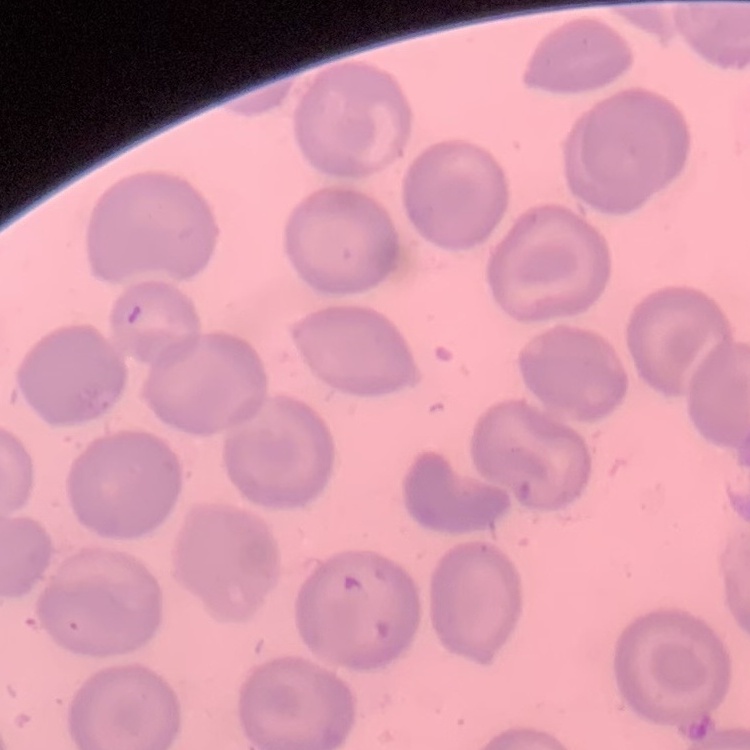
erythrocyte morphology = no rouleaux formation
preparation = thin blood film
image type = one tile cut from a larger photomicrograph
stain = Field's or Giemsa